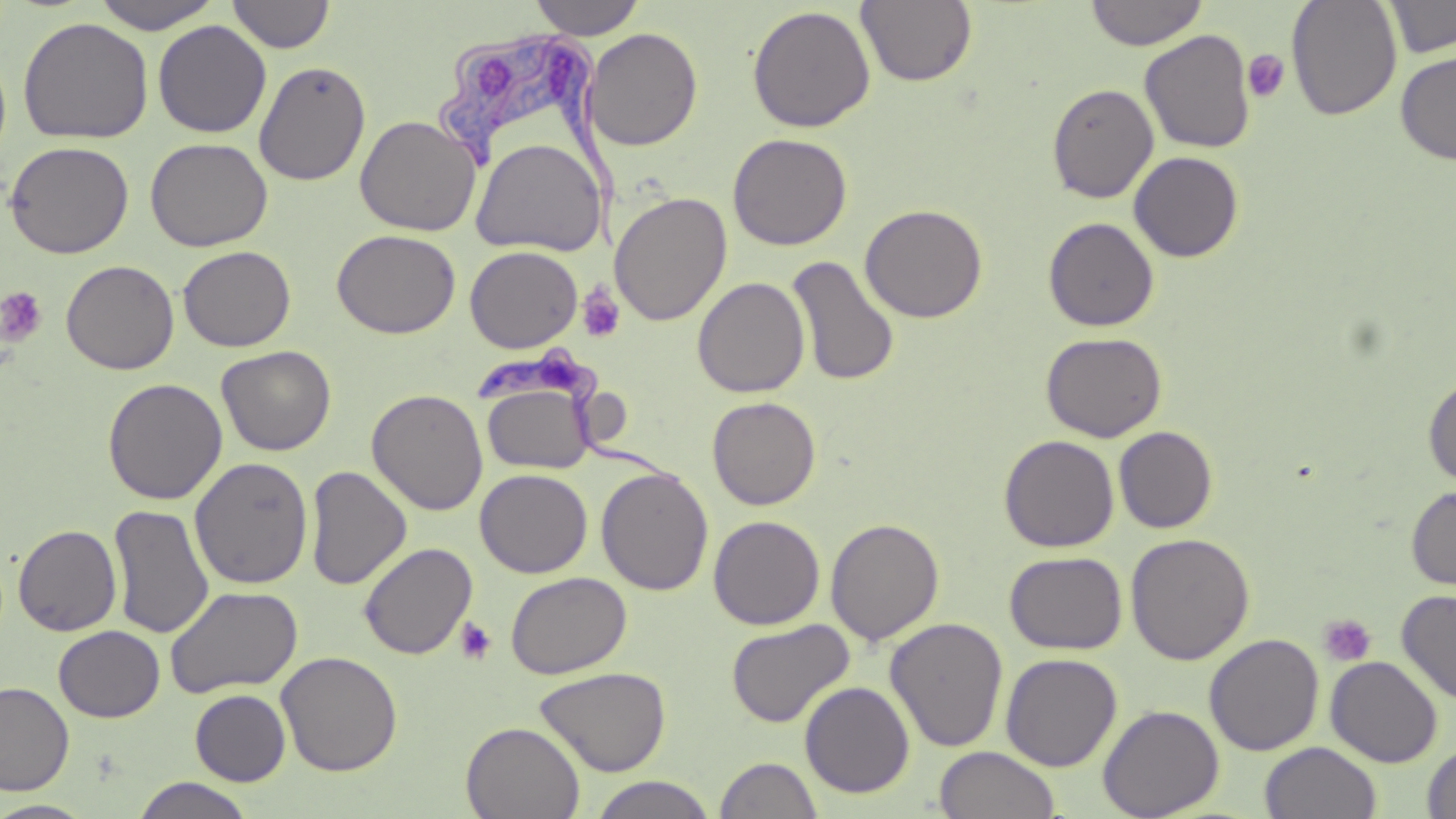
slide-level diagnosis = Trypanosoma brucei
image size = 1456×819 pixels
stain = May-Grünwald-Giemsa
field of view = single
magnification = 1000x
platelet locations = approximate bounding boxes as (x1,y1)-(x2,y2) corner pairs in pixels: (1242,49)-(1289,103), (0,286)-(48,348), (578,286)-(625,344), (1318,614)-(1376,667), (454,617)-(498,665)
Trypanosoma brucei locations = approximate bounding boxes as (x1,y1)-(x2,y2) corner pairs in pixels: (435,33)-(622,252), (473,345)-(682,488)
preparation = thin blood smear
modality = optical microscopy
uninfected red blood cell locations = approximate bounding boxes as (x1,y1)-(x2,y2) corner pairs in pixels: (91,0)-(225,33), (227,0)-(335,53), (527,0)-(647,39), (1084,0)-(1208,50), (1287,0)-(1403,121), (1383,0)-(1456,58), (855,1)-(978,87), (747,4)-(876,132), (18,16)-(153,144), (153,20)-(271,138), (584,28)-(703,151), (1139,29)-(1256,154), (1395,50)-(1456,166), (253,61)-(371,186), (1046,83)-(1159,203), (355,114)-(481,236), (728,133)-(852,250), (145,137)-(272,251), (471,137)-(605,256), (5,140)-(134,259), (1128,151)-(1244,263), (610,191)-(732,326), (860,203)-(988,323), (1043,216)-(1159,332), (332,229)-(461,338), (177,245)-(296,352), (465,245)-(583,353), (787,256)-(899,386), (61,259)-(179,375), (692,276)-(810,398), (1041,331)-(1168,442), (216,345)-(336,456), (1423,374)-(1456,489), (102,377)-(228,505), (483,383)-(595,474), (367,388)-(488,515), (707,396)-(821,510), (1114,426)-(1218,533), (999,434)-(1119,553), (190,456)-(313,589), (305,465)-(412,590), (596,467)-(713,596), (475,468)-(593,578), (1405,485)-(1456,592), (108,504)-(215,638), (708,514)-(825,630), (825,518)-(944,645), (13,524)-(122,636), (1125,532)-(1255,665), (358,542)-(478,660), (1004,551)-(1128,655), (505,571)-(632,678), (165,585)-(302,698), (1397,588)-(1456,707), (885,617)-(1009,752), (726,618)-(855,729), (53,625)-(165,722), (1204,633)-(1324,756), (276,651)-(403,776), (1000,653)-(1123,771), (1325,656)-(1443,767), (535,666)-(672,777), (0,680)-(76,796), (800,681)-(915,798), (190,689)-(291,785), (1098,704)-(1224,818), (461,721)-(585,819), (1259,741)-(1382,819), (1421,741)-(1456,818), (935,745)-(1061,819), (714,756)-(824,818), (130,776)-(256,818), (589,776)-(718,819), (0,800)-(99,818)